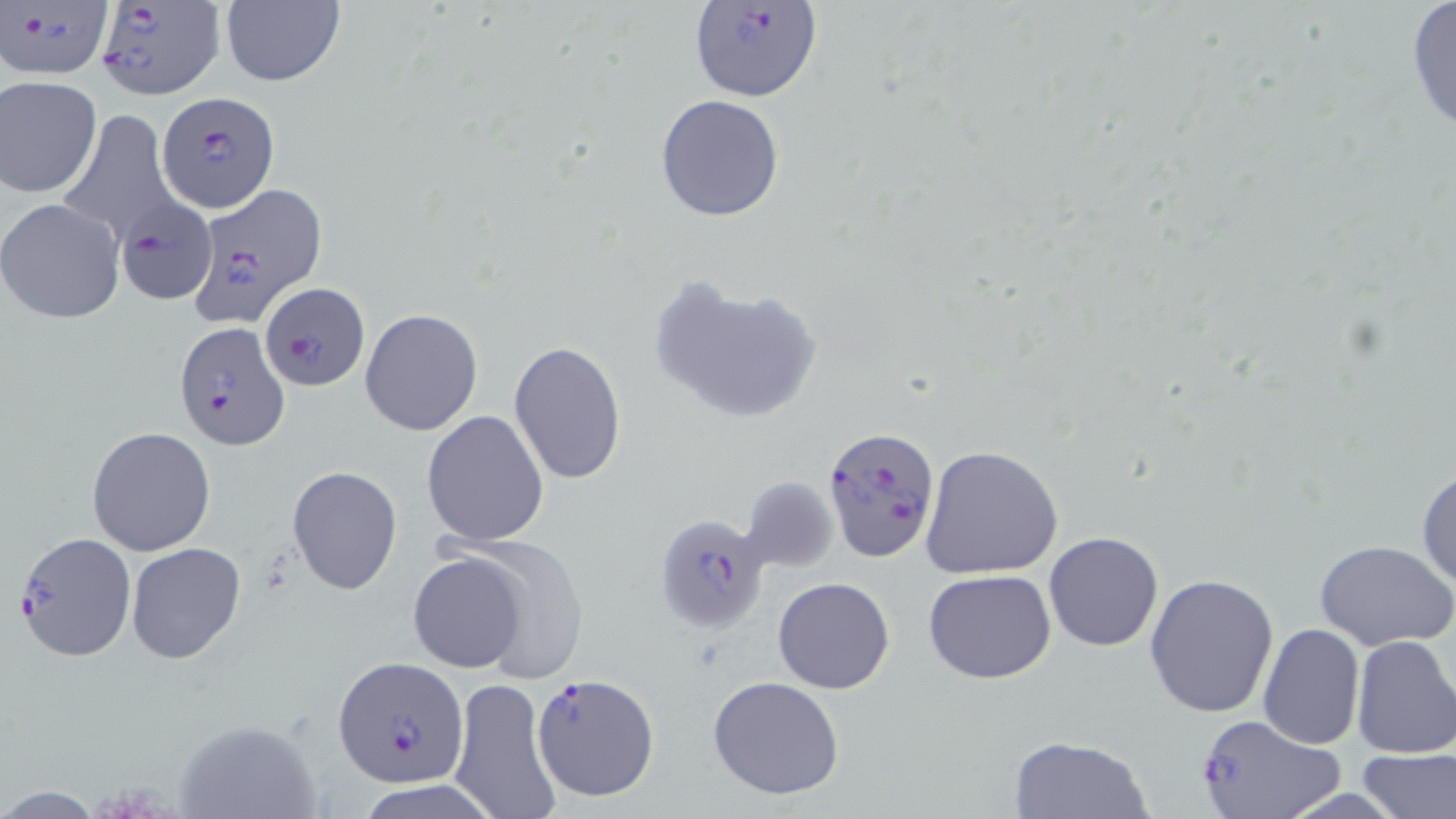
Approximate bounding boxes as named x1/y1/x2/y2 corners in pixels. Plasmodium falciparum-infected red blood cell locations: (x1=2, y1=0, x2=112, y2=80), (x1=94, y1=2, x2=227, y2=99), (x1=688, y1=3, x2=823, y2=104), (x1=156, y1=90, x2=281, y2=213), (x1=188, y1=180, x2=327, y2=329), (x1=116, y1=199, x2=215, y2=306), (x1=260, y1=283, x2=369, y2=390), (x1=171, y1=322, x2=288, y2=449), (x1=823, y1=426, x2=940, y2=563), (x1=656, y1=513, x2=771, y2=632), (x1=13, y1=531, x2=137, y2=663), (x1=333, y1=658, x2=470, y2=790), (x1=533, y1=672, x2=660, y2=801), (x1=1194, y1=712, x2=1347, y2=819). Uninfected red blood cell locations: (x1=1403, y1=1, x2=1456, y2=137), (x1=219, y1=2, x2=345, y2=87), (x1=0, y1=75, x2=102, y2=198), (x1=656, y1=94, x2=785, y2=222), (x1=57, y1=109, x2=181, y2=248), (x1=0, y1=198, x2=126, y2=324), (x1=649, y1=273, x2=823, y2=424), (x1=360, y1=309, x2=484, y2=436), (x1=508, y1=340, x2=627, y2=483), (x1=421, y1=409, x2=549, y2=547), (x1=87, y1=427, x2=217, y2=557), (x1=920, y1=444, x2=1064, y2=580), (x1=286, y1=465, x2=403, y2=595), (x1=1416, y1=466, x2=1456, y2=591), (x1=738, y1=476, x2=839, y2=574), (x1=1042, y1=532, x2=1164, y2=652), (x1=1314, y1=538, x2=1455, y2=650), (x1=441, y1=540, x2=590, y2=684), (x1=125, y1=542, x2=246, y2=664), (x1=408, y1=552, x2=530, y2=673), (x1=924, y1=569, x2=1057, y2=683), (x1=1145, y1=571, x2=1279, y2=718), (x1=772, y1=577, x2=895, y2=694), (x1=1258, y1=623, x2=1365, y2=749), (x1=1350, y1=634, x2=1456, y2=759), (x1=446, y1=676, x2=565, y2=818), (x1=706, y1=676, x2=846, y2=801), (x1=171, y1=716, x2=322, y2=819), (x1=1007, y1=734, x2=1154, y2=818), (x1=1356, y1=747, x2=1456, y2=819). Slide-level diagnosis: Plasmodium falciparum. Image is 1456×819 pixels. Light microscopy. May-Grünwald-Giemsa stain. 1000x magnification. Thin blood smear. One field of a larger specimen.